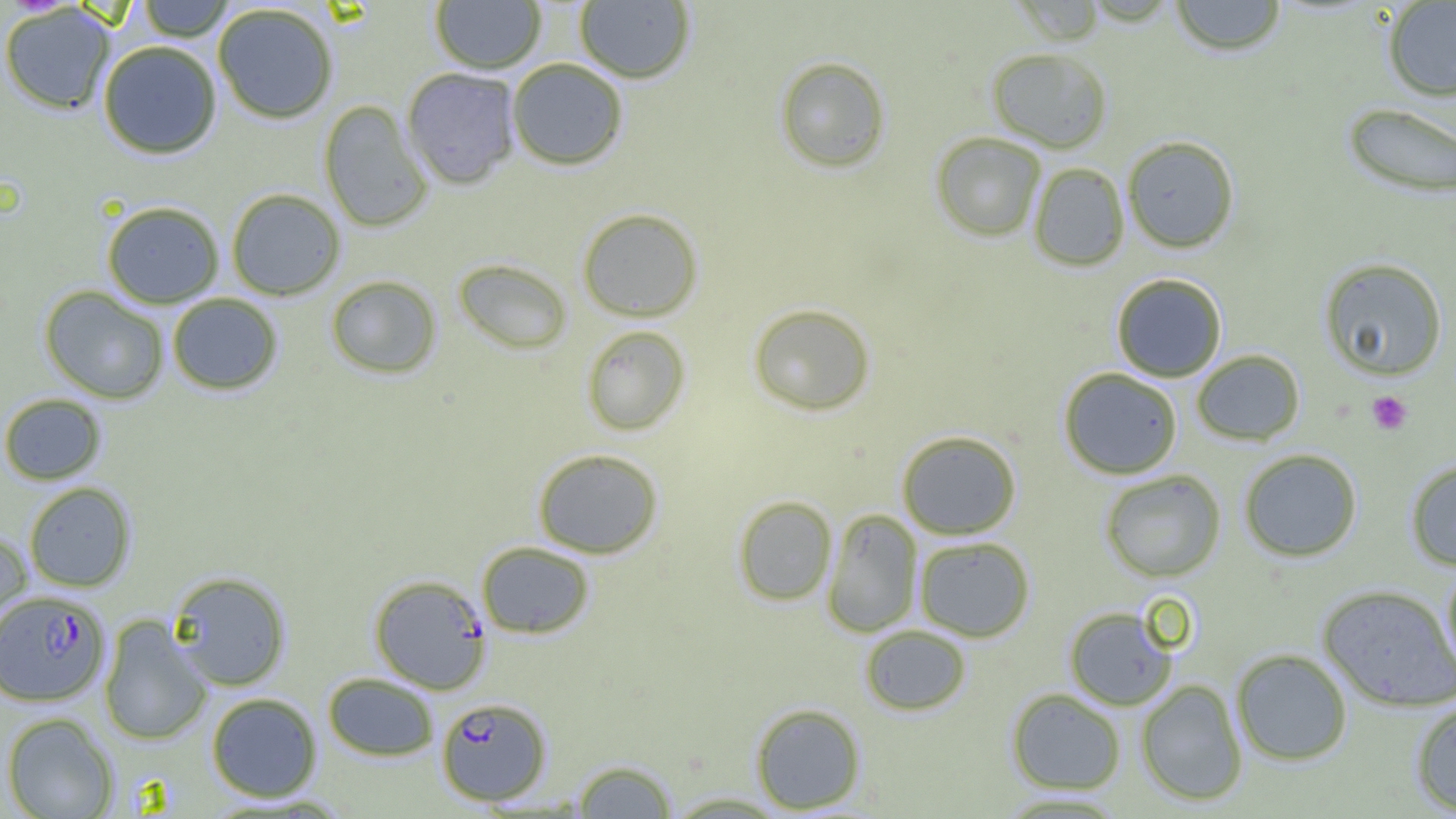
plasmodium_falciparum_infected_red_blood_cell_locations: 'approximate bounding boxes as [x1, y1, x2, y2] in pixels: [369, 574, 491, 694], [0, 590, 110, 706], [437, 697, 551, 805]'
slide_level_diagnosis: Plasmodium falciparum
uninfected_red_blood_cell_locations: 'approximate bounding boxes as [x1, y1, x2, y2] in pixels: [135, 0, 237, 42], [430, 0, 547, 74], [574, 0, 695, 83], [1013, 0, 1105, 45], [1169, 0, 1287, 56], [1382, 1, 1456, 102], [0, 3, 116, 115], [212, 4, 339, 124], [97, 40, 222, 159], [986, 47, 1113, 153], [774, 55, 891, 173], [506, 58, 628, 170], [402, 67, 521, 189], [318, 100, 433, 232], [1342, 101, 1456, 199], [931, 131, 1047, 241], [1121, 135, 1239, 253], [1028, 162, 1130, 271], [226, 188, 346, 300], [102, 201, 224, 308], [577, 207, 703, 322], [1319, 257, 1448, 380], [453, 258, 573, 354], [1111, 273, 1227, 382], [325, 275, 442, 379], [40, 286, 169, 404], [167, 293, 283, 395], [748, 303, 875, 415], [581, 325, 690, 436], [1191, 349, 1305, 445], [1058, 367, 1183, 480], [0, 393, 106, 485], [896, 430, 1022, 539], [533, 448, 664, 558], [1238, 448, 1362, 562], [1405, 459, 1456, 571], [1099, 469, 1226, 582], [24, 482, 136, 593], [733, 495, 837, 606], [822, 508, 923, 638], [0, 530, 32, 648], [913, 536, 1035, 642], [477, 541, 594, 639], [1442, 562, 1456, 678], [168, 571, 291, 691], [1317, 583, 1456, 711], [1064, 605, 1179, 711], [98, 615, 212, 746], [860, 625, 971, 716], [1230, 648, 1353, 765], [323, 673, 438, 760], [1135, 679, 1248, 806], [1006, 688, 1126, 795], [207, 693, 322, 802], [1410, 699, 1456, 816], [750, 703, 867, 813], [1, 712, 120, 818], [572, 759, 678, 818], [663, 791, 793, 817], [993, 791, 1130, 817]'
image_size: 1456×819 pixels
field_of_view: single
preparation: thin blood smear
modality: light microscopy
magnification: 1000x
platelet_locations: 'approximate bounding boxes as [x1, y1, x2, y2] in pixels: [1366, 390, 1413, 434]'